Outline each Plasmodium vivax-infected red blood cell.
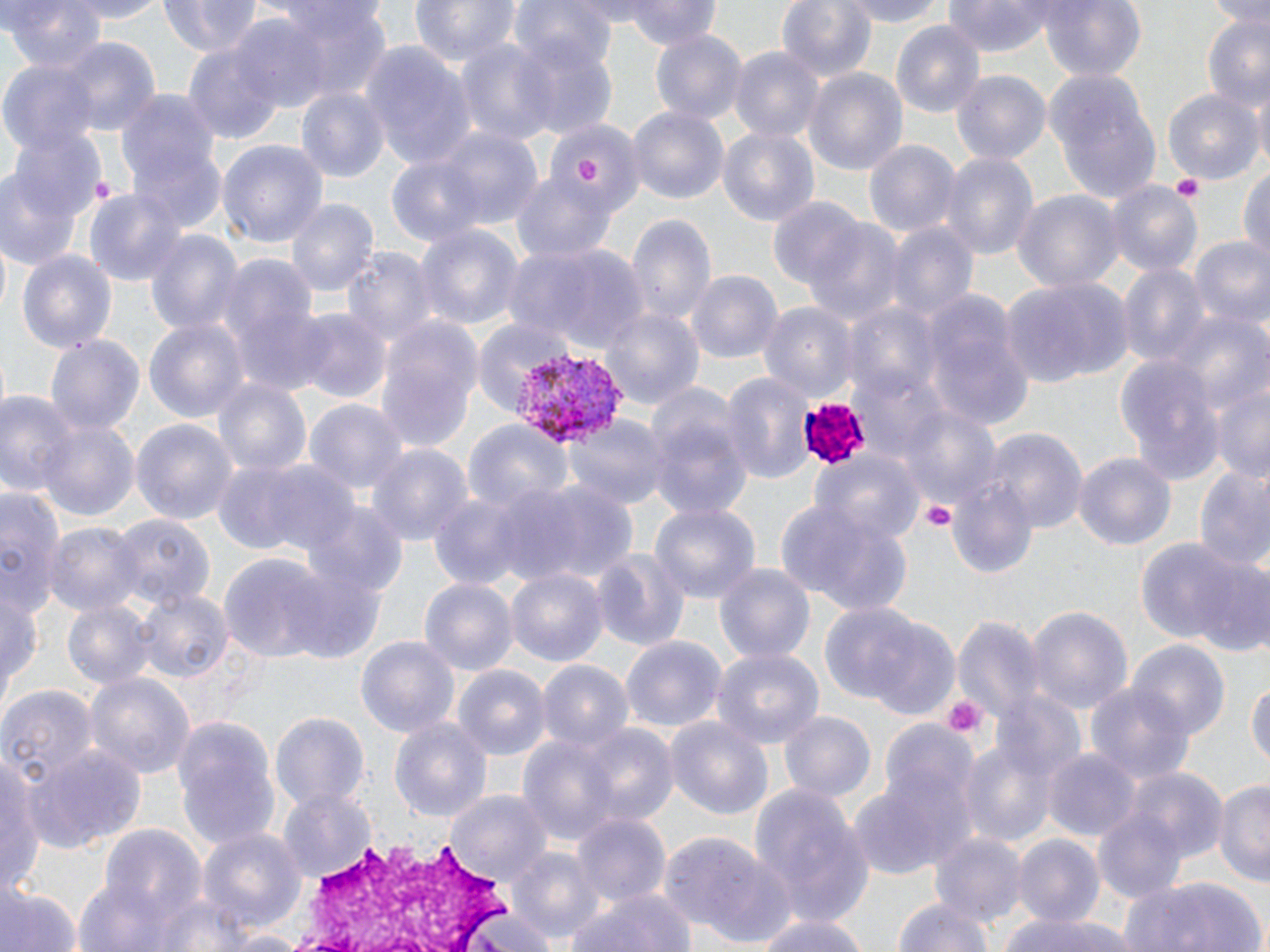
Approximate bounding boxes as [x1, y1, x2, y2] in pixels.
Plasmodium vivax-infected red blood cells: [516, 347, 624, 447].

slide-level diagnosis = Plasmodium vivax
image size = 1270×952 pixels
uninfected red blood cell locations = approximate bounding boxes as [x1, y1, x2, y2] in pixels: [2, 0, 108, 76], [53, 0, 175, 25], [160, 0, 262, 57], [410, 0, 520, 70], [509, 0, 620, 76], [621, 0, 721, 49], [778, 0, 879, 85], [846, 0, 946, 29], [943, 0, 1064, 54], [1038, 0, 1145, 84], [1204, 0, 1270, 25], [275, 5, 390, 103], [1197, 14, 1270, 108], [226, 16, 331, 114], [892, 19, 985, 120], [649, 28, 744, 127], [511, 30, 620, 139], [455, 35, 557, 147], [53, 37, 161, 139], [182, 39, 286, 147], [363, 43, 477, 169], [728, 45, 826, 141], [2, 62, 98, 151], [804, 67, 909, 179], [951, 68, 1054, 166], [1040, 70, 1166, 208], [295, 86, 390, 185], [114, 87, 224, 214], [1163, 88, 1264, 186], [628, 105, 728, 208], [549, 119, 644, 216], [717, 122, 820, 226], [427, 124, 546, 230], [7, 129, 107, 234], [130, 140, 229, 235], [218, 140, 328, 247], [865, 140, 959, 239], [941, 153, 1037, 262], [387, 155, 488, 249], [0, 165, 86, 268], [1238, 165, 1269, 261], [509, 169, 621, 266], [1105, 183, 1203, 282], [83, 186, 188, 290], [1013, 189, 1124, 294], [288, 198, 378, 297], [767, 199, 869, 295], [626, 211, 715, 328], [801, 216, 907, 326], [882, 218, 977, 324], [414, 223, 524, 334], [143, 227, 244, 340], [1188, 236, 1270, 330], [504, 240, 649, 354], [344, 246, 436, 352], [16, 247, 118, 357], [215, 257, 318, 367], [1117, 262, 1210, 369], [687, 269, 783, 365], [1005, 274, 1133, 387], [922, 293, 1035, 432], [760, 302, 858, 400], [845, 303, 945, 408], [604, 307, 704, 413], [293, 310, 389, 404], [1164, 310, 1267, 418], [144, 316, 249, 424], [376, 316, 481, 453], [468, 317, 578, 413], [45, 333, 147, 438], [1113, 352, 1225, 486], [849, 359, 953, 458], [1209, 366, 1270, 486], [721, 371, 813, 484], [212, 376, 309, 478], [0, 388, 81, 497], [305, 397, 407, 497], [644, 399, 754, 520], [895, 403, 1003, 516], [565, 415, 668, 511], [35, 416, 139, 526], [462, 417, 571, 516], [132, 418, 237, 530], [984, 428, 1087, 535], [366, 443, 472, 548], [811, 449, 923, 549], [1074, 451, 1177, 553], [215, 455, 356, 564], [1194, 467, 1270, 575], [947, 473, 1038, 579], [497, 478, 636, 588], [0, 484, 64, 620], [426, 492, 534, 591], [774, 498, 915, 614], [650, 501, 760, 605], [304, 504, 409, 602], [112, 512, 211, 615], [43, 521, 142, 619], [1136, 539, 1252, 651], [593, 547, 692, 656], [220, 554, 334, 665], [1193, 559, 1270, 656], [712, 560, 816, 665], [276, 566, 385, 662], [506, 570, 607, 666], [419, 577, 516, 674], [0, 586, 41, 706], [134, 587, 233, 686], [61, 598, 157, 693], [819, 604, 924, 706], [1026, 605, 1133, 718], [955, 617, 1044, 727], [869, 624, 960, 720], [620, 634, 727, 733], [355, 635, 461, 739], [1130, 639, 1228, 741], [711, 646, 824, 748], [538, 659, 632, 751], [452, 664, 549, 759], [84, 672, 194, 781], [1086, 679, 1195, 788], [1247, 680, 1270, 769], [0, 684, 99, 794], [995, 691, 1088, 790], [268, 711, 371, 812], [781, 711, 875, 804], [172, 716, 280, 850], [663, 716, 775, 824], [389, 717, 495, 826], [877, 717, 979, 838], [575, 723, 679, 831], [518, 734, 622, 849], [960, 735, 1057, 848], [24, 746, 145, 852], [1043, 746, 1139, 841], [2, 750, 41, 896], [1118, 764, 1229, 869], [1214, 779, 1269, 885], [846, 782, 955, 881], [748, 784, 875, 930], [276, 790, 375, 883], [449, 791, 551, 886], [1092, 806, 1190, 905], [571, 813, 674, 905], [94, 824, 208, 932], [197, 828, 304, 934], [931, 833, 1025, 930], [660, 835, 765, 931], [1012, 835, 1103, 930], [513, 849, 603, 943], [700, 851, 802, 950], [1119, 873, 1268, 952], [2, 883, 79, 952], [566, 889, 695, 952], [890, 895, 998, 952], [469, 908, 561, 952], [750, 910, 876, 952], [998, 911, 1136, 952], [217, 929, 311, 952]
modality = light microscopy
stain = May-Grünwald-Giemsa
white blood cell locations = approximate bounding boxes as [x1, y1, x2, y2] in pixels: [277, 839, 535, 949]
magnification = 1000x
field of view = single
preparation = thin blood film
platelet locations = approximate bounding boxes as [x1, y1, x2, y2] in pixels: [573, 154, 602, 185], [1172, 177, 1205, 205], [920, 499, 956, 529], [941, 695, 990, 744]